Describe the morphology of the erythrocytes.
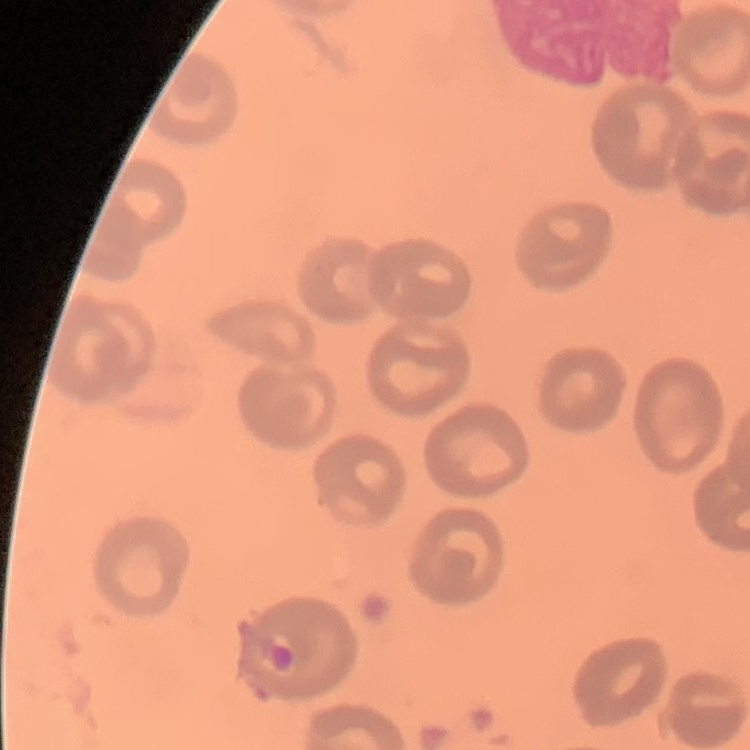

They show no rouleaux formation.

Summary:
  - Preparation: thin blood film
  - Image type: one tile cut from a larger photomicrograph
  - Stain: Field's or Giemsa